Give the extent of all Plasmodium vivax-infected red blood cells.
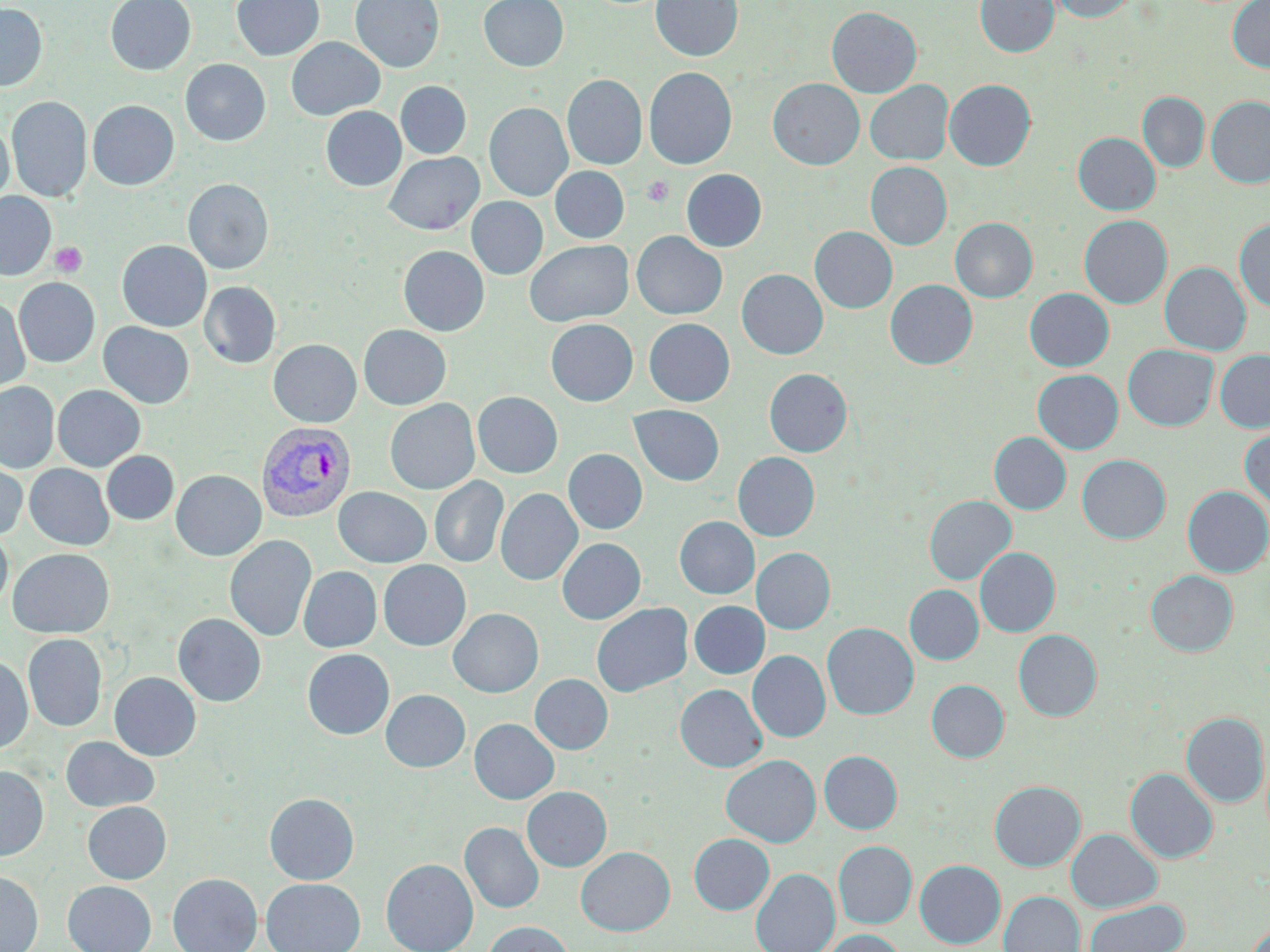

Approximate bounding boxes as (x1, y1, x2, y2) in pixels.
Plasmodium vivax-infected red blood cells: (256, 422, 356, 522).

slide-level diagnosis = Plasmodium vivax
stain = May-Grünwald-Giemsa
field of view = single
uninfected red blood cell locations = approximate bounding boxes as (x1, y1, x2, y2) in pixels: (105, 0, 196, 75), (231, 0, 324, 61), (351, 0, 445, 73), (479, 0, 568, 71), (652, 0, 742, 62), (975, 0, 1059, 57), (1048, 0, 1138, 22), (1228, 0, 1270, 73), (0, 3, 47, 91), (827, 6, 922, 97), (286, 37, 384, 120), (180, 59, 271, 146), (644, 67, 737, 169), (563, 74, 647, 169), (768, 78, 864, 169), (944, 79, 1036, 170), (865, 80, 953, 165), (396, 81, 471, 159), (1137, 92, 1209, 172), (7, 96, 92, 202), (1206, 96, 1270, 187), (87, 100, 179, 190), (485, 102, 572, 201), (321, 106, 405, 191), (0, 121, 14, 206), (1073, 132, 1160, 215), (384, 152, 483, 235), (866, 161, 952, 249), (551, 166, 629, 242), (681, 169, 767, 251), (183, 178, 274, 274), (0, 192, 56, 280), (466, 197, 548, 279), (1079, 215, 1172, 308), (950, 217, 1038, 302), (1234, 219, 1270, 312), (810, 227, 897, 313), (632, 231, 726, 319), (117, 240, 212, 331), (525, 240, 633, 327), (398, 246, 489, 336), (1160, 262, 1251, 355), (737, 269, 828, 359), (13, 278, 100, 367), (885, 279, 977, 369), (199, 281, 281, 368), (1025, 288, 1114, 371), (0, 298, 31, 396), (644, 318, 734, 406), (546, 319, 638, 406), (98, 322, 194, 408), (359, 325, 451, 410), (268, 339, 361, 427), (1123, 344, 1218, 431), (1215, 349, 1270, 432), (764, 368, 852, 456), (1033, 369, 1123, 454), (0, 382, 59, 472), (53, 385, 145, 471), (472, 391, 563, 478), (385, 399, 479, 495), (629, 405, 724, 486), (1240, 426, 1270, 512), (989, 432, 1071, 514), (564, 449, 647, 534), (102, 451, 178, 525), (733, 452, 819, 541), (1077, 454, 1171, 543), (0, 457, 27, 541), (25, 464, 114, 550), (171, 470, 266, 561), (430, 476, 509, 568), (1182, 485, 1270, 577), (333, 487, 432, 567), (496, 488, 582, 585), (924, 495, 1016, 584), (675, 516, 759, 599), (0, 528, 13, 612), (225, 535, 317, 642), (557, 538, 645, 624), (752, 547, 835, 634), (976, 547, 1060, 636), (8, 548, 114, 638), (378, 560, 471, 650), (298, 566, 382, 652), (1145, 570, 1238, 657), (905, 584, 984, 664), (689, 601, 769, 678), (592, 603, 692, 697), (448, 608, 543, 697), (173, 613, 266, 706), (822, 622, 918, 719), (1013, 629, 1102, 721), (22, 634, 107, 732), (302, 649, 394, 740), (748, 650, 830, 742), (0, 655, 33, 754), (109, 672, 201, 760), (530, 674, 613, 754), (926, 679, 1009, 762), (676, 684, 767, 772), (381, 690, 470, 772), (1182, 712, 1269, 806), (470, 718, 559, 804), (60, 736, 160, 812), (819, 750, 902, 833), (721, 754, 821, 847), (0, 765, 48, 860), (1125, 767, 1218, 863), (989, 780, 1085, 871), (522, 786, 611, 871), (264, 792, 359, 884), (82, 802, 171, 884), (460, 822, 545, 913), (1066, 828, 1162, 912), (689, 833, 774, 914), (833, 840, 917, 928), (576, 846, 675, 936), (381, 858, 478, 952), (914, 860, 1005, 948), (751, 868, 839, 952), (0, 871, 43, 952), (168, 873, 262, 952), (262, 878, 365, 952), (63, 880, 156, 952), (999, 891, 1085, 952), (1084, 900, 1188, 952), (481, 921, 576, 952), (1246, 922, 1270, 952), (818, 929, 907, 952)
image size = 1270×952 pixels
platelet locations = approximate bounding boxes as (x1, y1, x2, y2) in pixels: (641, 175, 674, 207), (50, 242, 88, 277)
preparation = thin blood film
magnification = 1000x
modality = light microscopy